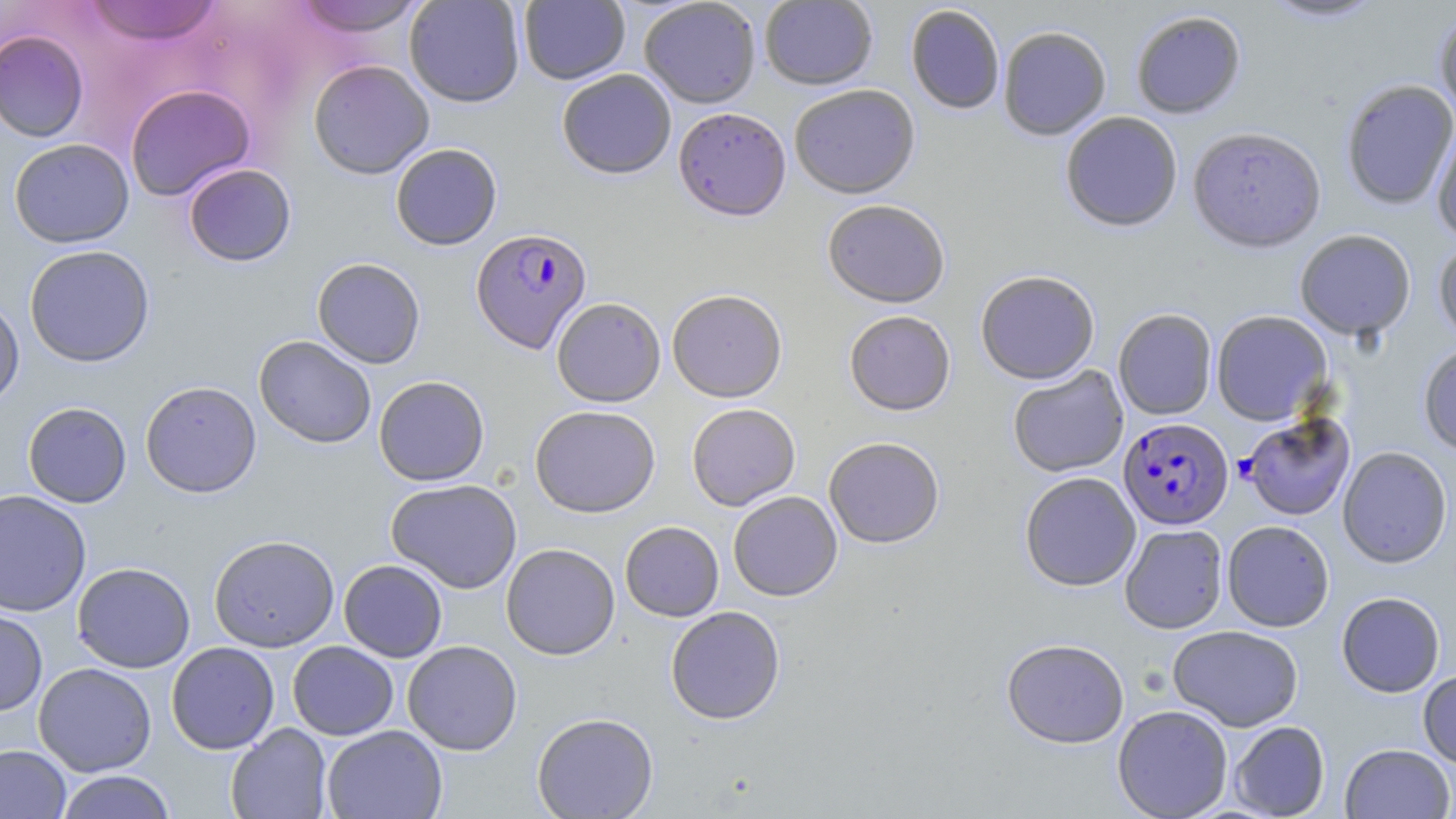 Approximate bounding boxes as (x1, y1, x2, y2) in pixels. Plasmodium falciparum-infected red blood cell locations: (471, 227, 592, 353), (1239, 413, 1356, 521), (1118, 417, 1232, 530). Uninfected red blood cell locations: (291, 0, 430, 37), (404, 0, 525, 107), (519, 0, 630, 84), (760, 0, 878, 90), (1258, 0, 1388, 25), (83, 1, 223, 46), (639, 1, 761, 108), (905, 5, 1005, 115), (1130, 11, 1247, 119), (1434, 11, 1456, 124), (998, 26, 1111, 141), (0, 29, 89, 142), (308, 60, 434, 179), (557, 69, 676, 179), (1340, 79, 1456, 210), (125, 84, 255, 201), (789, 85, 920, 199), (673, 107, 791, 221), (1060, 112, 1183, 233), (1431, 119, 1456, 244), (1187, 127, 1326, 253), (9, 138, 134, 248), (390, 143, 502, 250), (183, 163, 297, 267), (822, 199, 950, 307), (1295, 230, 1416, 341), (1434, 238, 1456, 346), (24, 245, 155, 368), (311, 258, 426, 369), (975, 270, 1100, 384), (667, 289, 787, 402), (0, 294, 25, 410), (552, 297, 666, 407), (1113, 309, 1217, 420), (844, 310, 955, 415), (1211, 310, 1332, 425), (254, 335, 377, 448), (1418, 343, 1456, 457), (1007, 365, 1128, 478), (374, 376, 490, 486), (140, 381, 262, 498), (23, 402, 131, 508), (686, 403, 801, 510), (529, 405, 661, 517), (824, 437, 945, 549), (1337, 446, 1452, 568), (1020, 471, 1141, 591), (386, 479, 522, 594), (0, 490, 92, 617), (728, 491, 843, 601), (1222, 520, 1334, 632), (620, 521, 724, 621), (1119, 524, 1228, 634), (208, 534, 340, 652), (501, 543, 620, 660), (339, 559, 447, 662), (72, 562, 195, 673), (1336, 592, 1445, 698), (665, 606, 785, 724), (0, 609, 48, 716), (1168, 625, 1304, 731), (1002, 638, 1129, 748), (402, 640, 522, 755), (287, 641, 399, 740), (166, 642, 279, 754), (33, 662, 157, 776), (1417, 670, 1456, 768), (1112, 704, 1233, 818), (532, 712, 658, 818), (1228, 721, 1330, 818), (226, 724, 332, 819), (322, 725, 447, 819), (1339, 743, 1454, 818), (0, 745, 71, 819), (55, 770, 177, 819). Slide-level diagnosis: Plasmodium falciparum. Light microscopy. Thin blood smear. Captured at 1000x magnification. One field of a larger specimen. Image is 1456×819 pixels. May-Grünwald-Giemsa stain.